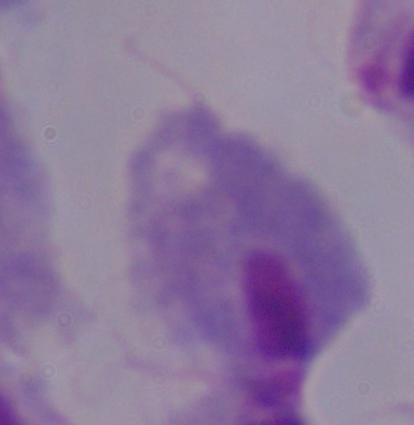
modality: photomicrograph
magnification: 1000x
identification: trichomonad